Classify this cell by malaria status.
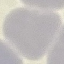
Uninfected.

stain = Giemsa
capture = smartphone through the microscope eyepiece
image type = automatically extracted cell patch, resized to 64 × 64 pixels
preparation = thin blood film